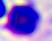
Summary:
  - Identification: leukocyte
  - Modality: micrograph
  - Magnification: 400x